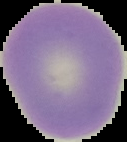 From a thin blood smear. Result: no malaria parasites seen. Image is 127×142 pixels. Cell region segmented out of the field of view; the surrounding area is masked to black.